Name the parasite shown.
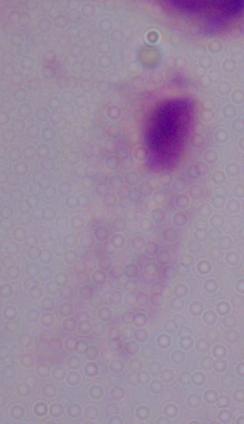

This is a trichomonad.

Summary:
  - Magnification: 1000x
  - Modality: micrograph